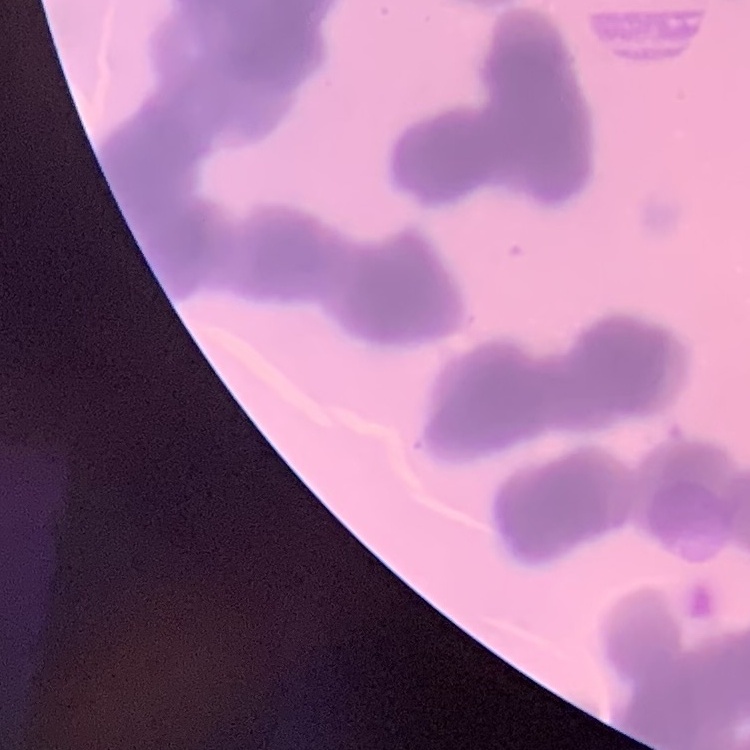
red blood cell morphology = rouleaux formation
image type = square crop of a larger photomicrograph
stain = Field's or Giemsa
preparation = thin blood smear